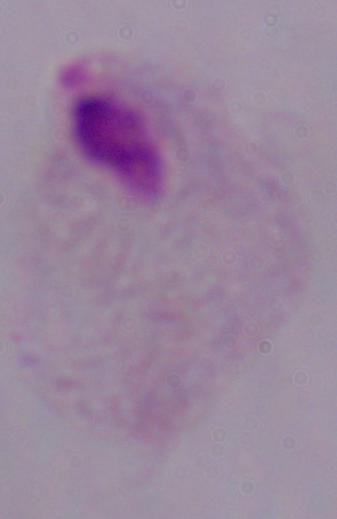

magnification: 1000x
modality: photomicrograph
identification: trichomonad